Comment on the morphology of the red blood cells.
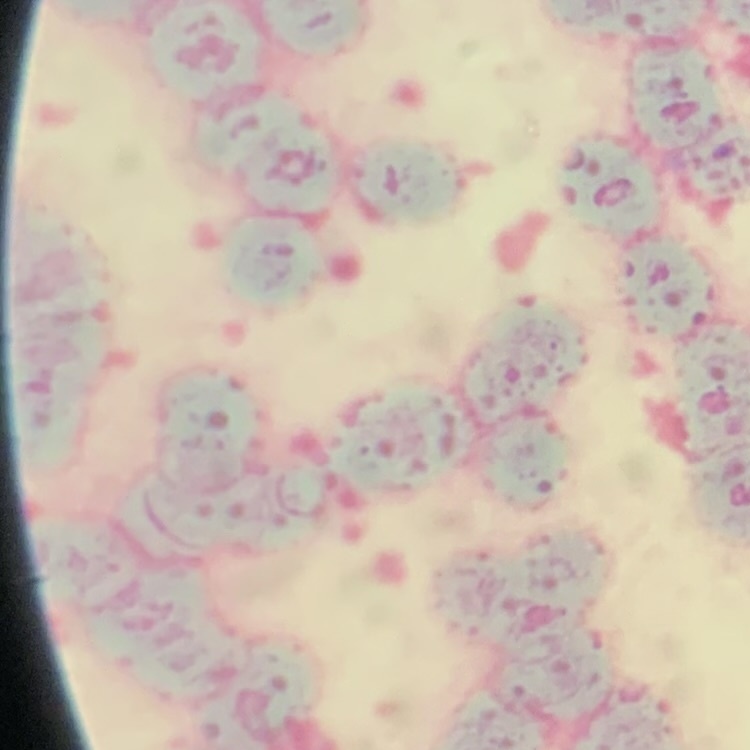
Rouleaux formation.

Summary:
  - Image type: one tile cut from a larger photomicrograph
  - Preparation: thin peripheral smear
  - Stain: Field's or Giemsa